State which cell type is depicted.
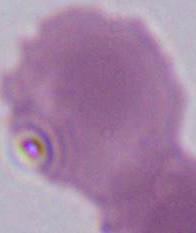

An erythrocyte.

Photomicrograph. 1000x magnification.